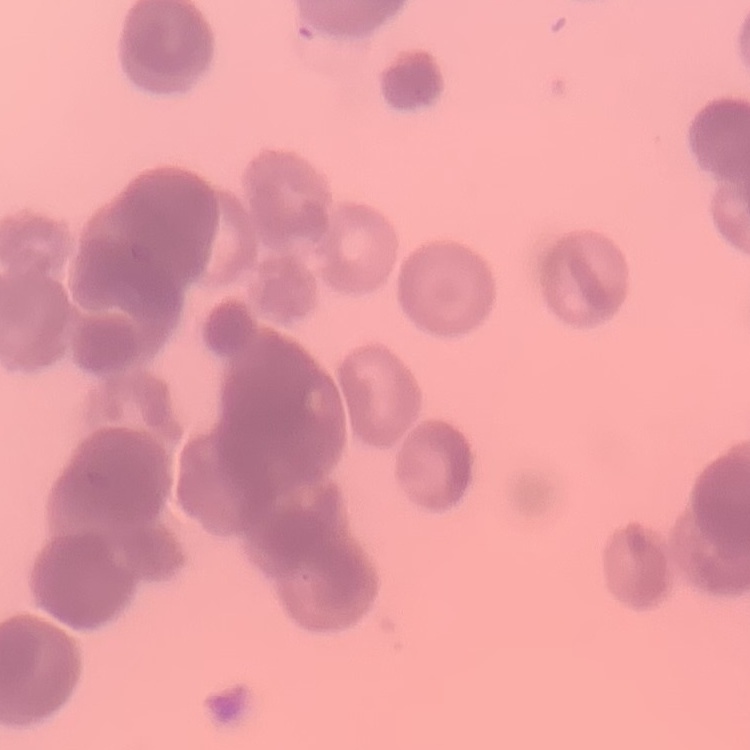
{
  "red_blood_cell_morphology": "rouleaux formation",
  "image_type": "square crop of a larger photomicrograph",
  "preparation": "thin blood film",
  "stain": "Field's or Giemsa"
}